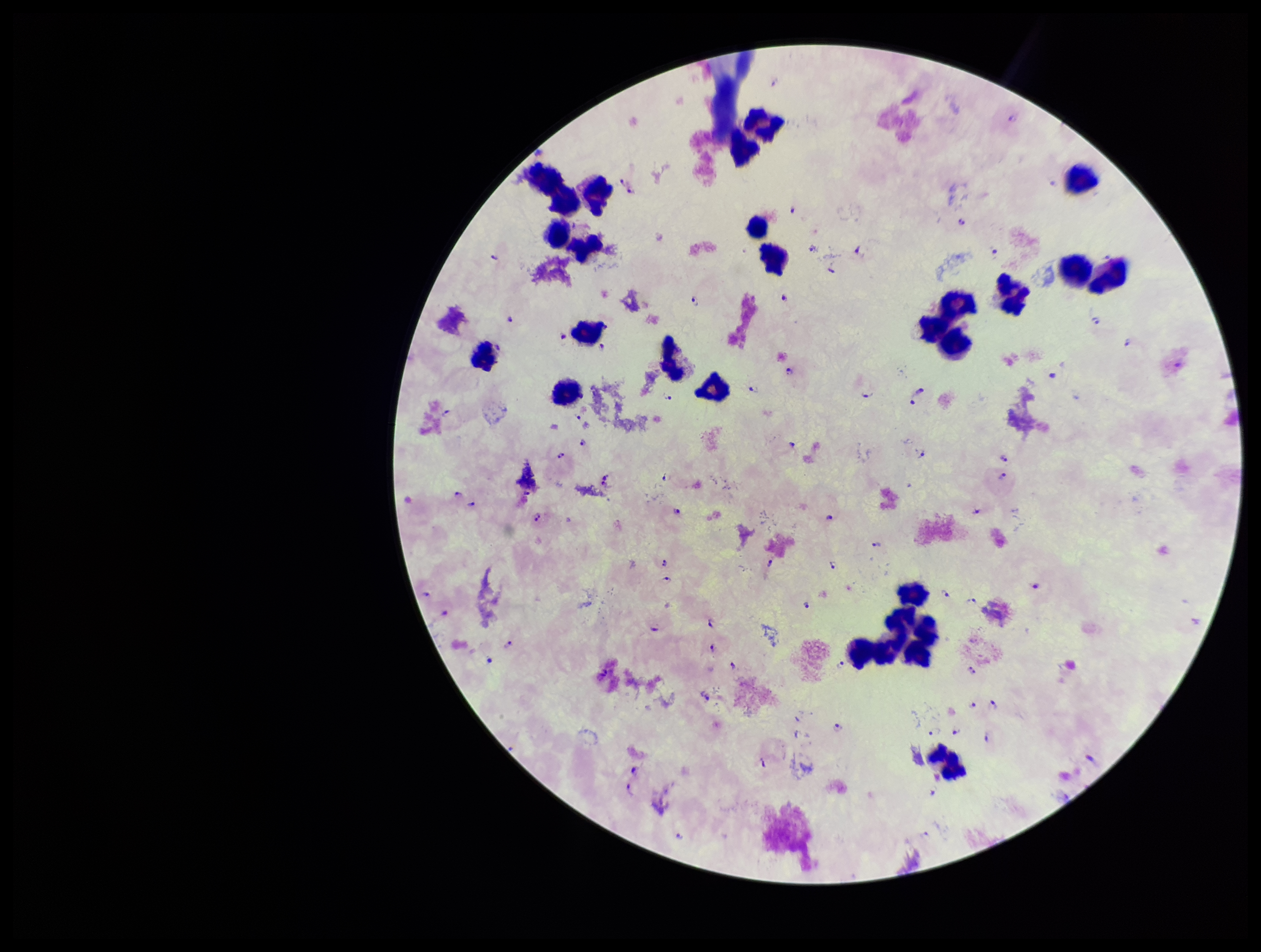
field of view = single
species reported for this patient = Plasmodium falciparum
image size = 1261×952 pixels
preparation = thick smear
stain = Giemsa
parasite count = 80
Plasmodium parasites = seen
capture = smartphone photograph through the microscope eyepiece
leukocyte count = 24
patient malaria status = infected